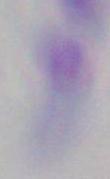
Photomicrograph. Toxoplasma gondii is shown. Captured at 1000x magnification.